Report the malaria status of this cell.
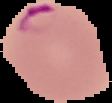
Parasitized.

From a thin blood film. Image is 112×103 pixels. Segmented cell region on a black background.